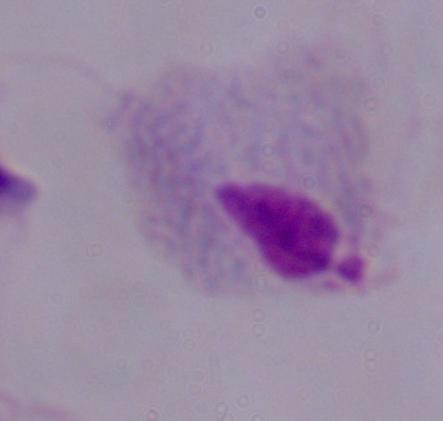
modality: micrograph
magnification: 1000x
identification: trichomonad